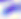

modality: micrograph
magnification: 400x
identification: Toxoplasma gondii